Assess the morphology of the erythrocytes.
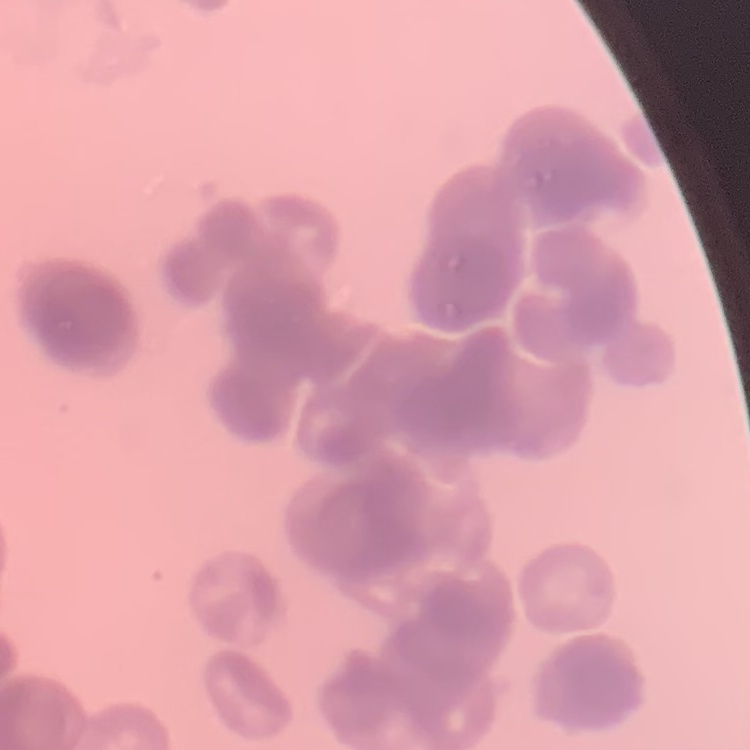
They show rouleaux formation.

stain = Field's or Giemsa
preparation = thin blood smear
image type = square crop of a larger photomicrograph